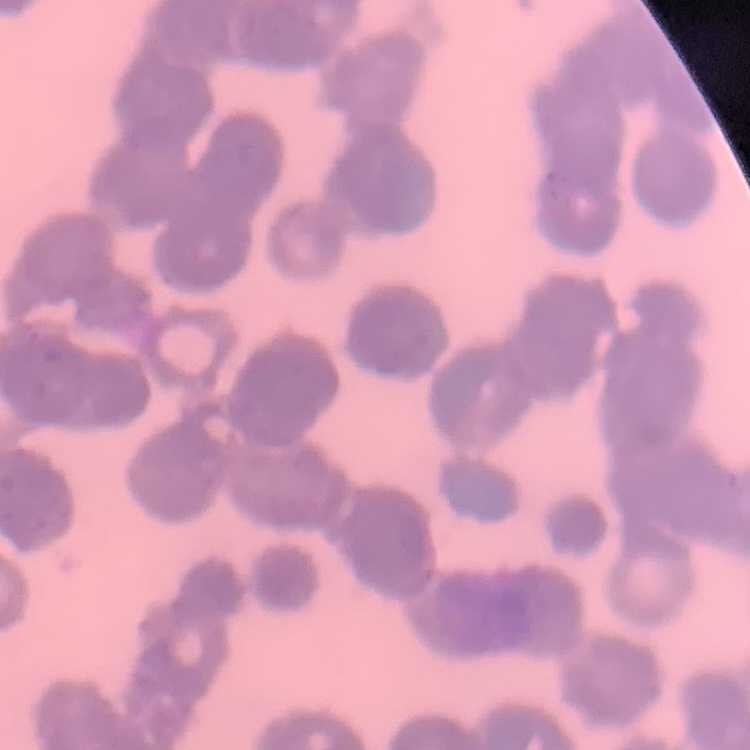
Summary:
  - Red blood cell morphology: rouleaux formation
  - Stain: Field's or Giemsa
  - Image type: one tile cut from a larger photomicrograph
  - Preparation: thin blood film